Name the blood parasite species.
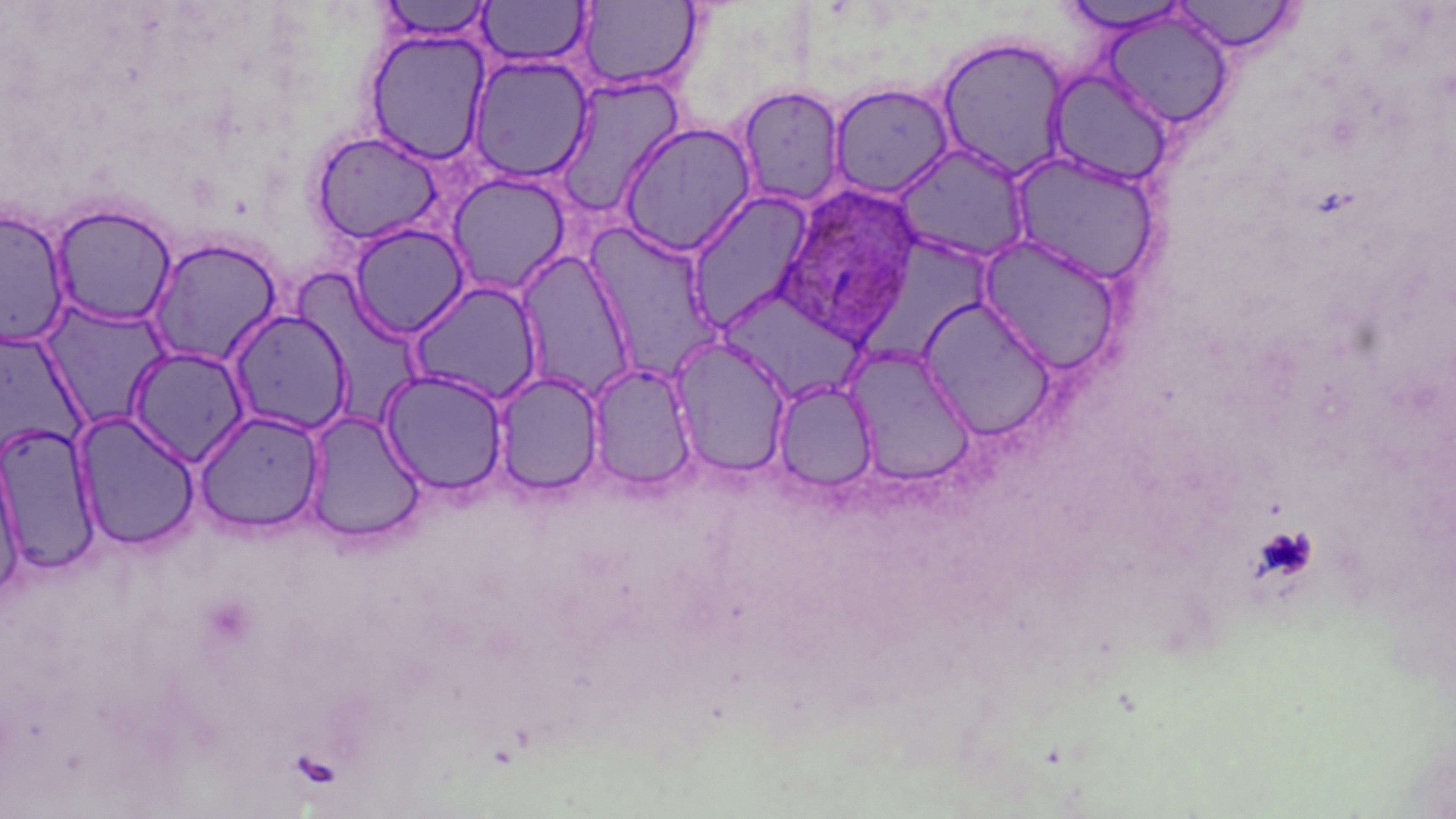

Plasmodium ovale.

image size = 1456×819 pixels
preparation = thin blood smear
magnification = 1000x
field of view = single
modality = light microscopy
Plasmodium ovale-infected red blood cell locations = approximate bounding boxes as (x1,y1)-(x2,y2) corner pairs in pixels: (769,182)-(920,348)
stain = May-Grünwald-Giemsa
platelet locations = approximate bounding boxes as (x1,y1)-(x2,y2) corner pairs in pixels: (1252,526)-(1318,583)
uninfected red blood cell locations = approximate bounding boxes as (x1,y1)-(x2,y2) corner pairs in pixels: (1167,0)-(1305,55), (376,1)-(495,42), (478,1)-(592,68), (575,1)-(705,94), (1054,1)-(1196,35), (1101,11)-(1236,131), (364,28)-(493,165), (934,35)-(1072,181), (467,53)-(594,183), (1046,67)-(1175,187), (552,75)-(688,216), (829,83)-(955,199), (734,84)-(847,209), (617,121)-(757,257), (309,129)-(446,246), (892,143)-(1031,265), (1007,150)-(1162,286), (445,172)-(572,297), (685,191)-(816,333), (50,204)-(178,327), (0,208)-(72,348), (348,222)-(472,339), (583,222)-(726,382), (977,234)-(1125,376), (145,236)-(284,369), (514,248)-(639,403), (405,279)-(546,407), (716,285)-(867,404), (916,296)-(1057,441), (43,306)-(172,432), (225,308)-(354,436), (670,337)-(792,478), (126,346)-(251,467), (843,346)-(977,487), (586,362)-(698,494), (379,369)-(510,496), (493,371)-(604,497), (772,379)-(877,493), (192,409)-(326,535), (303,410)-(426,545), (72,411)-(201,552), (0,420)-(102,576), (0,449)-(26,604)